Name the parasite shown.
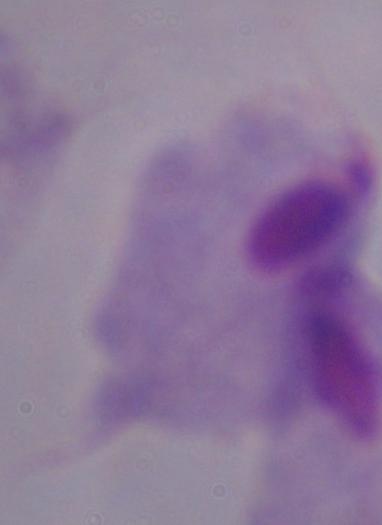

A trichomonad.

Captured at 1000x magnification. Photomicrograph.